Identify the blood parasite species.
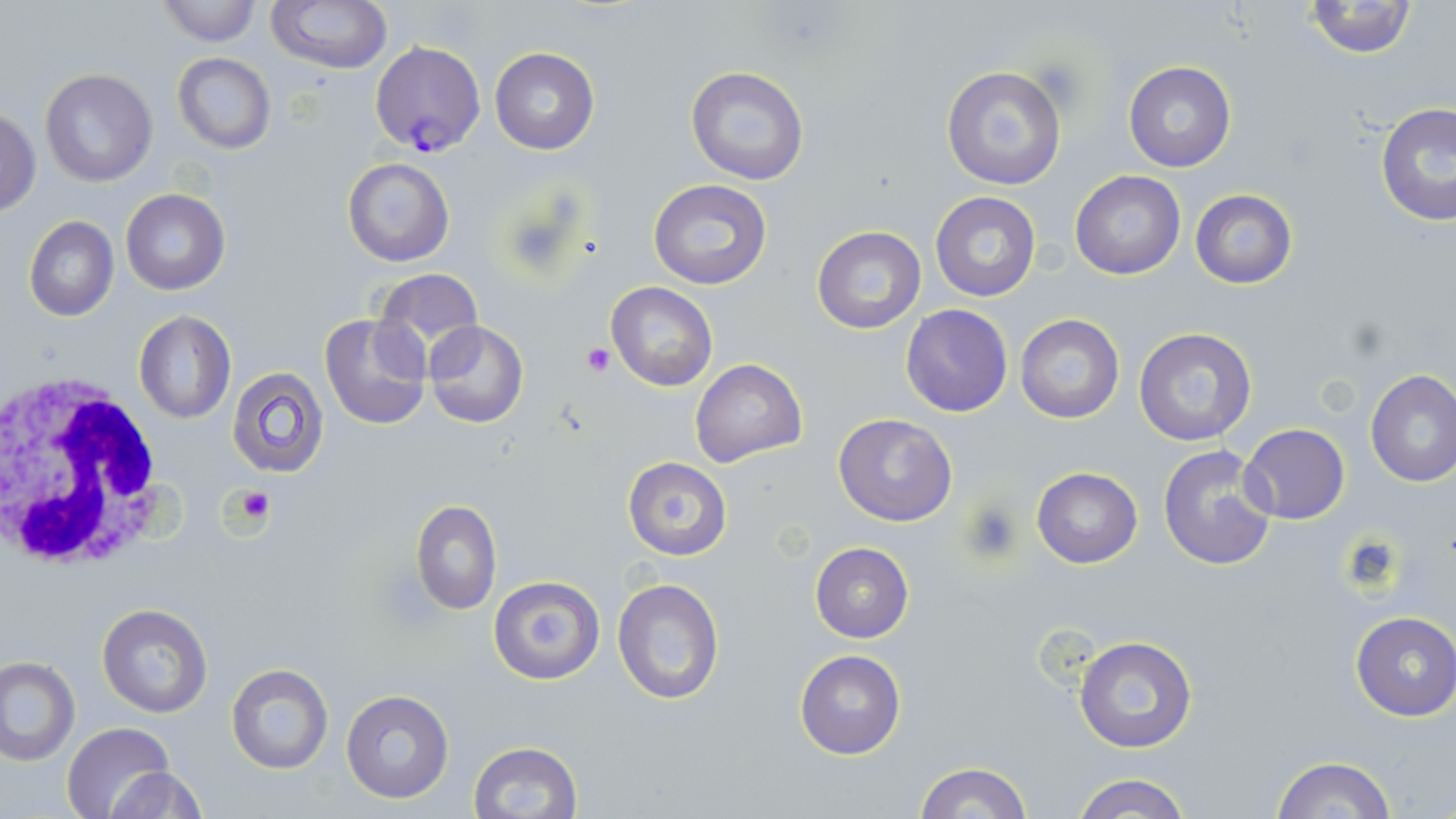
Plasmodium falciparum.

white blood cell locations = approximate bounding boxes as (x1, y1, x2, y2) in pixels: (1, 369, 172, 575)
Plasmodium falciparum-infected red blood cell locations = approximate bounding boxes as (x1, y1, x2, y2) in pixels: (371, 39, 484, 158)
magnification = 1000x
image size = 1456×819 pixels
stain = May-Grünwald-Giemsa
field of view = one of a larger specimen
preparation = thin blood smear
platelet locations = approximate bounding boxes as (x1, y1, x2, y2) in pixels: (1034, 57, 1085, 109), (581, 342, 615, 375), (230, 484, 276, 527), (962, 499, 1024, 563), (1339, 534, 1407, 594)
uninfected red blood cell locations = approximate bounding boxes as (x1, y1, x2, y2) in pixels: (267, 0, 391, 72), (1302, 0, 1418, 58), (153, 1, 262, 48), (490, 47, 598, 154), (172, 53, 276, 154), (1123, 61, 1236, 171), (942, 64, 1068, 191), (686, 65, 811, 186), (40, 67, 159, 187), (1374, 103, 1456, 226), (1, 108, 41, 215), (343, 158, 454, 267), (1069, 170, 1186, 279), (649, 179, 771, 290), (121, 187, 231, 295), (1190, 189, 1297, 289), (930, 191, 1041, 302), (24, 215, 118, 322), (811, 226, 926, 333), (371, 269, 484, 359), (606, 282, 718, 392), (900, 305, 1012, 416), (133, 311, 237, 424), (318, 313, 432, 432), (1014, 314, 1125, 423), (423, 320, 529, 428), (1132, 326, 1259, 449), (690, 358, 807, 467), (227, 365, 330, 479), (1365, 370, 1456, 487), (833, 412, 957, 526), (1238, 424, 1350, 525), (1156, 444, 1279, 571), (622, 456, 732, 561), (1032, 467, 1143, 568), (410, 499, 501, 615), (810, 541, 913, 642), (611, 575, 724, 708), (487, 577, 606, 685), (96, 602, 213, 717), (1350, 611, 1456, 721), (1074, 636, 1197, 752), (794, 650, 905, 759), (1, 657, 79, 763), (224, 662, 334, 775), (341, 688, 453, 804), (63, 721, 175, 819), (467, 741, 582, 819), (1270, 757, 1398, 818), (914, 762, 1034, 818), (103, 766, 207, 819), (1069, 773, 1195, 819)
modality = optical microscopy